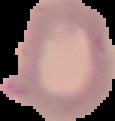
image type = segmented cell region on a black background
image size = 115×121 pixels
preparation = thin blood film
malaria status = uninfected